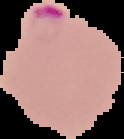 Image is 124×139 pixels. Cell region segmented out of the field of view; the surrounding area is masked to black. From a thin blood film. Malaria status: parasitized.